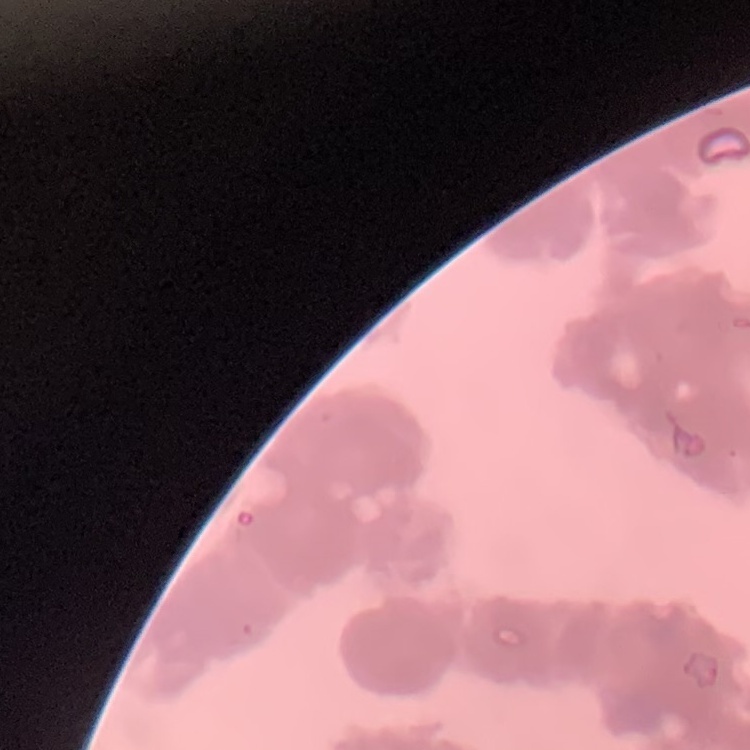

erythrocyte morphology = rouleaux formation
preparation = thin blood film
stain = Field's or Giemsa
image type = one tile cut from a larger photomicrograph